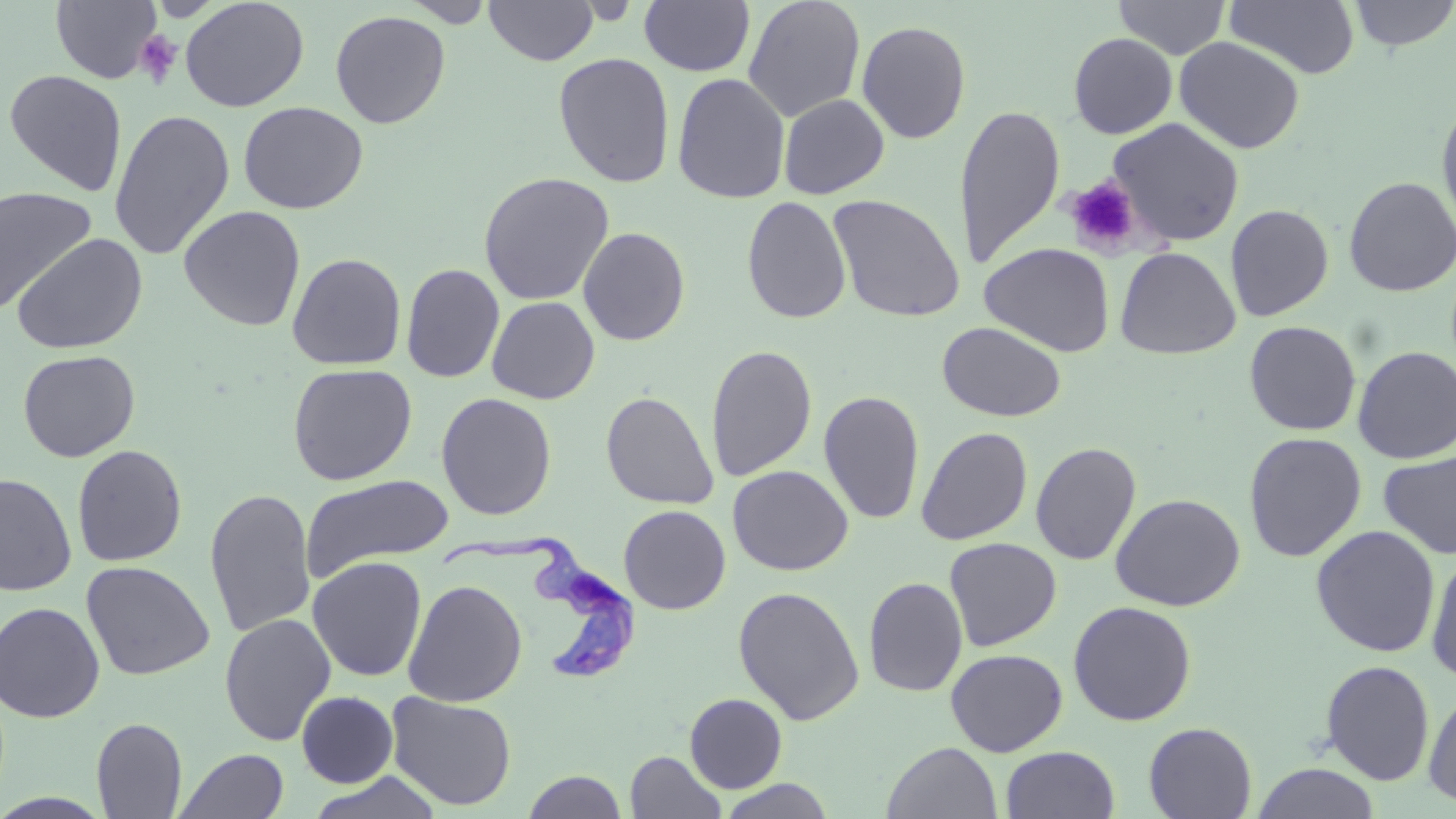

Approximate bounding boxes as (x1,y1)-(x2,y2) corner pairs in pixels. Platelet locations: (135,31)-(182,87), (1064,177)-(1142,255). Uninfected red blood cell locations: (51,0)-(162,84), (179,0)-(309,112), (743,0)-(865,122), (1113,0)-(1230,59), (1224,0)-(1361,80), (1346,0)-(1456,52), (399,1)-(497,26), (483,1)-(599,66), (639,1)-(755,77), (330,10)-(451,129), (857,21)-(971,144), (1068,33)-(1178,139), (1174,36)-(1305,154), (553,53)-(675,188), (4,69)-(128,196), (672,72)-(791,204), (778,94)-(889,199), (1436,95)-(1456,239), (238,102)-(368,214), (954,104)-(1065,270), (108,109)-(235,261), (1106,118)-(1245,246), (478,172)-(615,306), (1343,176)-(1456,297), (0,187)-(98,312), (828,194)-(965,323), (741,196)-(852,324), (1225,204)-(1334,322), (179,205)-(306,331), (577,226)-(691,346), (12,233)-(148,354), (980,242)-(1116,357), (1115,247)-(1241,360), (287,252)-(406,370), (401,263)-(505,383), (486,296)-(600,404), (937,321)-(1066,422), (1244,321)-(1362,436), (706,344)-(817,482), (1352,346)-(1456,464), (17,349)-(140,461), (287,363)-(417,485), (819,390)-(925,525), (601,391)-(718,509), (436,392)-(557,520), (916,426)-(1033,545), (1243,432)-(1367,562), (1030,441)-(1142,565), (71,444)-(188,567), (1378,450)-(1456,560), (727,465)-(853,575), (0,472)-(77,597), (300,474)-(454,581), (204,487)-(316,637), (1109,493)-(1246,611), (619,505)-(731,614), (1311,525)-(1440,657), (944,537)-(1062,651), (1425,548)-(1456,683), (307,556)-(427,681), (81,561)-(215,681), (863,577)-(968,697), (403,579)-(527,707), (733,585)-(865,726), (0,601)-(105,723), (1068,601)-(1196,726), (219,613)-(336,746), (945,649)-(1068,756), (1320,660)-(1435,785), (1422,685)-(1456,808), (296,691)-(399,787), (386,691)-(517,811), (684,693)-(787,793), (91,716)-(187,818), (1143,722)-(1257,818), (882,742)-(1002,818), (1001,746)-(1120,819), (176,749)-(289,819), (625,751)-(726,818), (1252,762)-(1381,819), (522,770)-(627,818), (305,771)-(444,818), (714,778)-(837,818). Trypanosoma brucei locations: (444,537)-(639,682). Slide-level diagnosis: Trypanosoma brucei. Single field of view. May-Grünwald-Giemsa stain. Light microscopy. 1000x magnification. Image is 1456×819 pixels. Thin blood film.